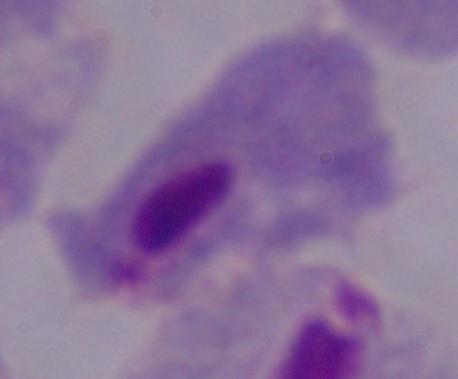

modality = photomicrograph
magnification = 1000x
identification = trichomonad